Look for Plasmodium parasites.
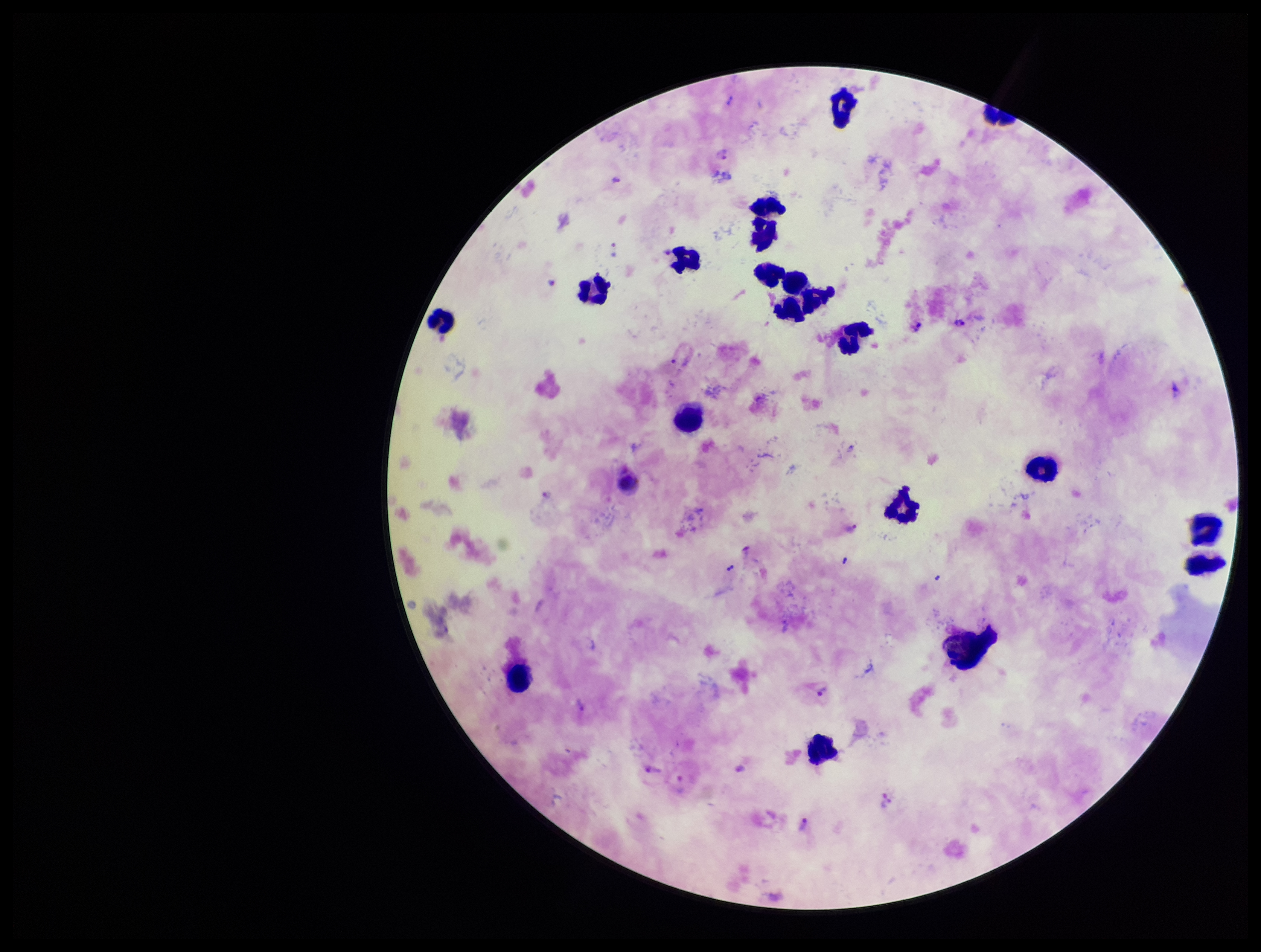
Identified.

field of view = single
preparation = thick
stain = Giemsa
patient malaria status = positive
leukocyte count = 20
image size = 1261×952 pixels
capture = smartphone photograph through the microscope eyepiece
parasite count = 11
species reported for this patient = Plasmodium vivax